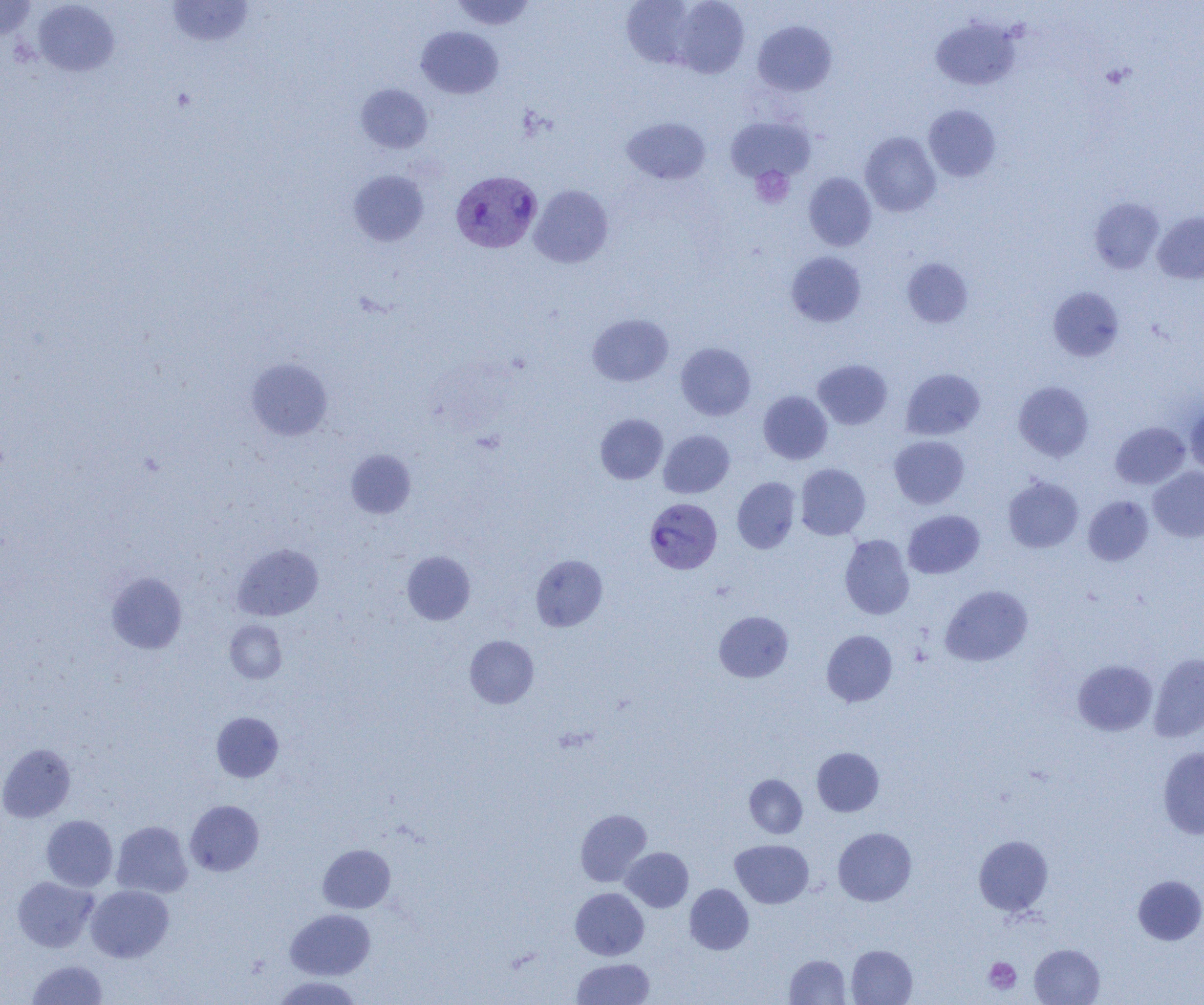

slide-level diagnosis = Plasmodium vivax
magnification = 1000x
preparation = thin blood smear
modality = light microscopy
uninfected red blood cell locations = approximate bounding boxes as named x1/y1/x2/y2 corners in pixels: (x1=0, y1=0, x2=38, y2=39), (x1=166, y1=0, x2=255, y2=48), (x1=450, y1=0, x2=537, y2=31), (x1=671, y1=0, x2=749, y2=78), (x1=33, y1=1, x2=120, y2=77), (x1=622, y1=1, x2=699, y2=69), (x1=931, y1=18, x2=1020, y2=90), (x1=753, y1=19, x2=836, y2=96), (x1=416, y1=26, x2=503, y2=99), (x1=355, y1=83, x2=433, y2=153), (x1=923, y1=105, x2=1001, y2=182), (x1=724, y1=116, x2=815, y2=184), (x1=622, y1=117, x2=710, y2=184), (x1=860, y1=132, x2=940, y2=217), (x1=348, y1=170, x2=428, y2=246), (x1=804, y1=173, x2=877, y2=251), (x1=529, y1=185, x2=613, y2=268), (x1=1089, y1=197, x2=1164, y2=274), (x1=1153, y1=211, x2=1204, y2=284), (x1=786, y1=252, x2=866, y2=327), (x1=902, y1=258, x2=973, y2=328), (x1=1048, y1=287, x2=1124, y2=362), (x1=588, y1=314, x2=673, y2=386), (x1=676, y1=343, x2=756, y2=420), (x1=246, y1=358, x2=333, y2=441), (x1=813, y1=359, x2=892, y2=429), (x1=901, y1=368, x2=984, y2=440), (x1=1013, y1=381, x2=1094, y2=462), (x1=758, y1=390, x2=833, y2=464), (x1=1185, y1=401, x2=1204, y2=476), (x1=596, y1=413, x2=667, y2=484), (x1=1110, y1=422, x2=1190, y2=489), (x1=658, y1=429, x2=734, y2=498), (x1=889, y1=435, x2=969, y2=509), (x1=346, y1=449, x2=416, y2=518), (x1=796, y1=464, x2=870, y2=540), (x1=1148, y1=467, x2=1204, y2=542), (x1=1003, y1=476, x2=1083, y2=552), (x1=732, y1=477, x2=801, y2=553), (x1=1083, y1=495, x2=1154, y2=566), (x1=902, y1=510, x2=984, y2=579), (x1=839, y1=534, x2=914, y2=619), (x1=232, y1=544, x2=322, y2=620), (x1=402, y1=551, x2=475, y2=625), (x1=530, y1=555, x2=607, y2=631), (x1=107, y1=572, x2=187, y2=654), (x1=940, y1=585, x2=1033, y2=666), (x1=714, y1=611, x2=793, y2=682), (x1=225, y1=620, x2=288, y2=683), (x1=821, y1=630, x2=897, y2=706), (x1=465, y1=635, x2=539, y2=708), (x1=1149, y1=653, x2=1204, y2=741), (x1=1073, y1=660, x2=1157, y2=735), (x1=211, y1=712, x2=283, y2=782), (x1=0, y1=743, x2=76, y2=822), (x1=812, y1=747, x2=884, y2=816), (x1=1158, y1=747, x2=1204, y2=838), (x1=745, y1=775, x2=807, y2=838), (x1=185, y1=800, x2=264, y2=876), (x1=575, y1=809, x2=652, y2=886), (x1=41, y1=815, x2=118, y2=891), (x1=111, y1=821, x2=193, y2=898), (x1=833, y1=827, x2=916, y2=906), (x1=973, y1=835, x2=1053, y2=915), (x1=730, y1=839, x2=814, y2=908), (x1=317, y1=844, x2=395, y2=913), (x1=622, y1=847, x2=693, y2=912), (x1=1133, y1=875, x2=1204, y2=945), (x1=12, y1=876, x2=98, y2=952), (x1=685, y1=884, x2=753, y2=954), (x1=86, y1=885, x2=174, y2=962), (x1=571, y1=887, x2=649, y2=960), (x1=285, y1=909, x2=375, y2=980), (x1=1029, y1=944, x2=1104, y2=1005), (x1=847, y1=945, x2=917, y2=1004), (x1=785, y1=954, x2=850, y2=1004), (x1=572, y1=958, x2=654, y2=1004), (x1=27, y1=959, x2=108, y2=1005), (x1=271, y1=976, x2=362, y2=1004)
field of view = one of a larger specimen
platelet locations = approximate bounding boxes as named x1/y1/x2/y2 corners in pixels: (x1=750, y1=165, x2=794, y2=208), (x1=983, y1=957, x2=1021, y2=994)
Plasmodium vivax-infected red blood cell locations = approximate bounding boxes as named x1/y1/x2/y2 corners in pixels: (x1=450, y1=170, x2=542, y2=253), (x1=644, y1=497, x2=722, y2=574)
image size = 1204×1005 pixels